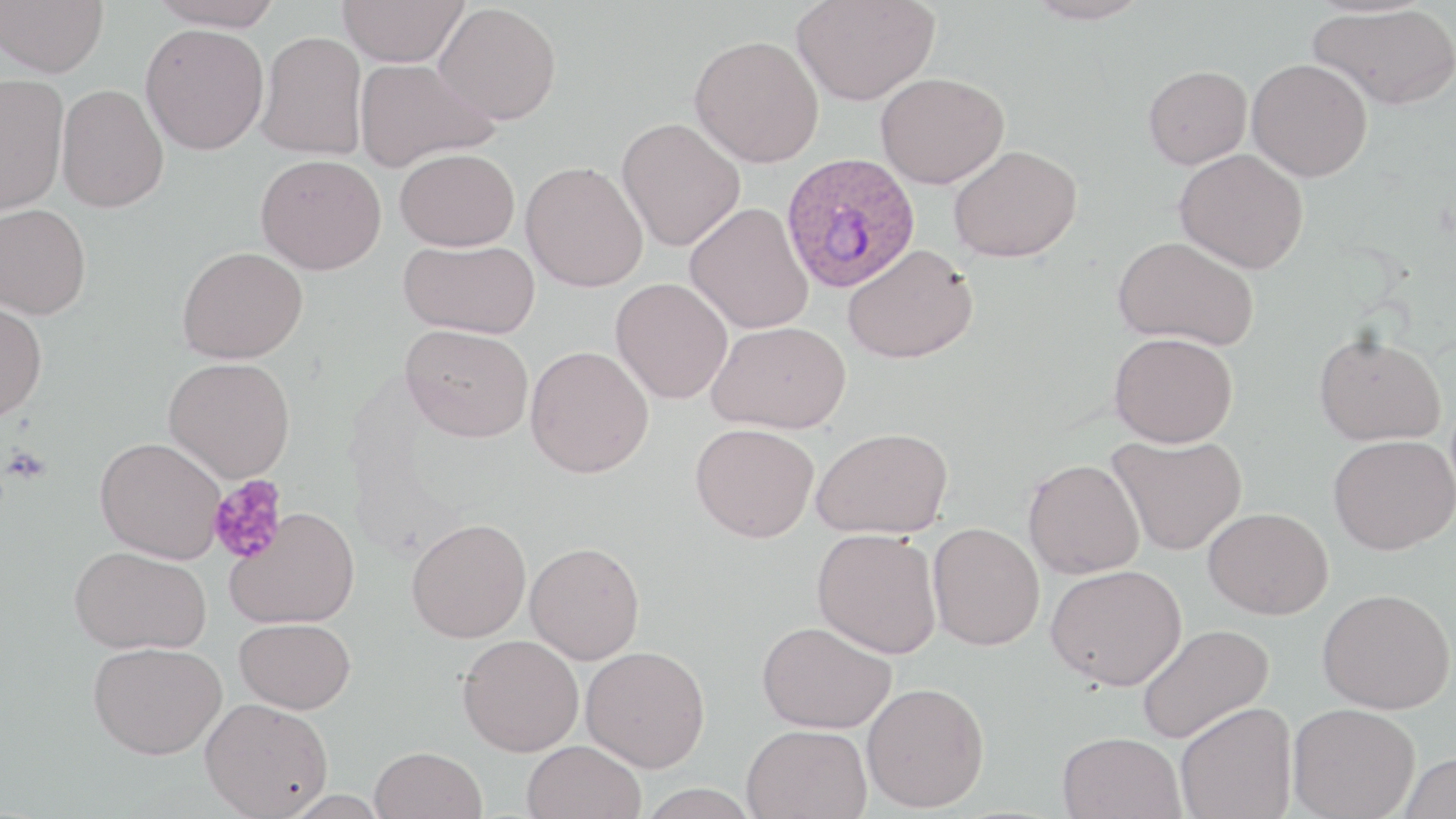
Approximate bounding boxes as (x1,y1)-(x2,y2) corner pairs in pixels. Platelet locations: (3,446)-(50,484), (208,475)-(289,564). Uninfected red blood cell locations: (0,0)-(108,77), (148,0)-(284,30), (338,0)-(469,67), (792,0)-(940,106), (1025,0)-(1151,25), (434,3)-(562,124), (1309,4)-(1456,110), (140,23)-(270,154), (255,30)-(368,160), (689,34)-(824,168), (353,58)-(498,172), (1246,58)-(1373,181), (1143,66)-(1252,169), (0,72)-(70,215), (875,72)-(1008,188), (57,83)-(169,212), (616,117)-(745,252), (949,144)-(1082,263), (395,147)-(520,251), (1174,149)-(1308,273), (255,153)-(386,274), (520,160)-(649,292), (685,202)-(814,334), (0,203)-(92,319), (1113,235)-(1260,350), (399,239)-(540,339), (842,243)-(978,364), (177,245)-(308,364), (610,277)-(733,404), (0,299)-(47,422), (706,320)-(851,434), (401,324)-(534,442), (1109,332)-(1238,447), (1314,332)-(1446,446), (525,345)-(654,478), (163,356)-(295,482), (690,423)-(819,542), (812,427)-(953,539), (1107,433)-(1247,555), (1328,434)-(1456,555), (95,436)-(226,562), (1023,458)-(1145,579), (225,507)-(361,629), (1204,507)-(1333,620), (406,518)-(532,643), (928,521)-(1045,650), (812,529)-(943,658), (525,541)-(645,664), (69,544)-(212,654), (1046,565)-(1187,691), (1318,587)-(1455,714), (235,617)-(355,714), (756,620)-(897,733), (1136,623)-(1274,744), (458,635)-(584,756), (88,641)-(227,759), (580,645)-(710,771), (861,682)-(990,812), (200,698)-(333,818), (1175,701)-(1297,819), (1287,704)-(1420,819), (742,723)-(871,818), (1058,731)-(1185,819), (521,740)-(647,819), (370,746)-(487,819), (1399,751)-(1455,819). Plasmodium ovale-infected red blood cell locations: (780,150)-(921,293). Slide-level diagnosis: Plasmodium ovale. Thin blood film. One field of a larger specimen. Light microscopy. Image is 1456×819 pixels. May-Grünwald-Giemsa stain. 1000x magnification.